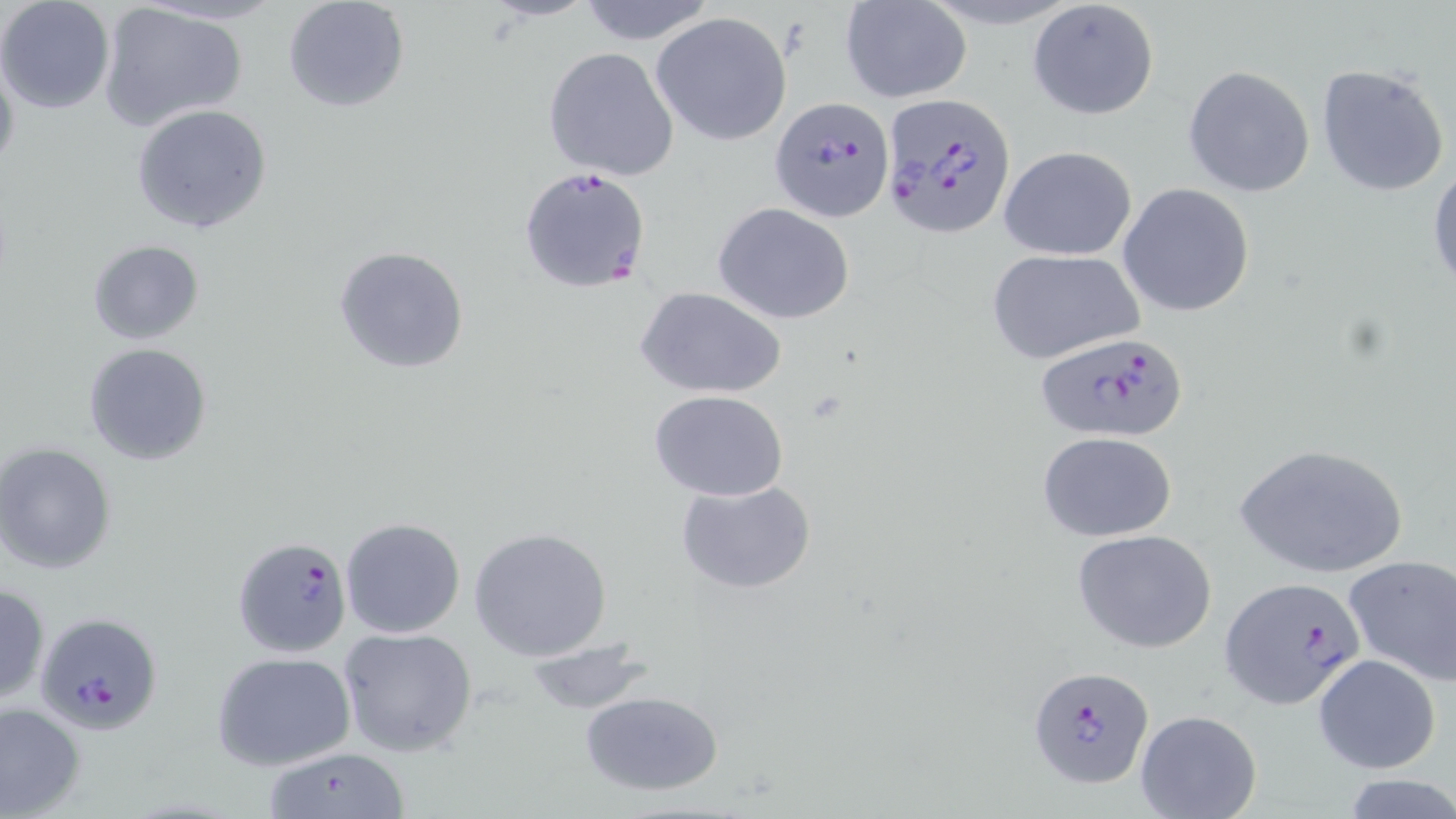
Approximate bounding boxes as [x1, y1, x2, y2] in pixels. Plasmodium falciparum-infected red blood cell locations: [881, 94, 1015, 236], [770, 97, 893, 222], [519, 166, 651, 294], [1035, 331, 1187, 443], [231, 534, 351, 657], [1219, 577, 1368, 709], [34, 612, 164, 735], [1028, 664, 1155, 790]. Uninfected red blood cell locations: [282, 0, 410, 114], [571, 0, 720, 46], [840, 0, 971, 103], [0, 1, 116, 114], [1027, 1, 1160, 120], [95, 2, 248, 132], [651, 12, 791, 145], [543, 46, 679, 182], [0, 48, 21, 182], [1315, 63, 1451, 198], [1182, 65, 1315, 196], [132, 103, 273, 234], [999, 146, 1136, 260], [1428, 160, 1456, 298], [1117, 183, 1257, 317], [713, 203, 854, 324], [86, 240, 205, 346], [333, 245, 472, 375], [987, 249, 1142, 365], [636, 288, 784, 398], [81, 341, 213, 467], [647, 390, 790, 500], [1038, 431, 1178, 542], [1231, 442, 1410, 579], [1, 443, 119, 575], [675, 479, 818, 596], [340, 517, 467, 639], [467, 527, 614, 662], [1071, 529, 1218, 654], [1341, 554, 1456, 688], [0, 582, 50, 705], [337, 626, 479, 757], [524, 638, 652, 714], [211, 652, 356, 772], [1312, 654, 1441, 774], [579, 690, 727, 797], [0, 700, 85, 818], [1135, 710, 1261, 819], [258, 748, 412, 819], [1338, 776, 1456, 817]. Slide-level diagnosis: Plasmodium falciparum. Single field of view. Captured at 1000x magnification. Thin blood smear. Optical microscopy. May-Grünwald-Giemsa-stained preparation. Image is 1456×819 pixels.